Outline each blood parasite and name the species.
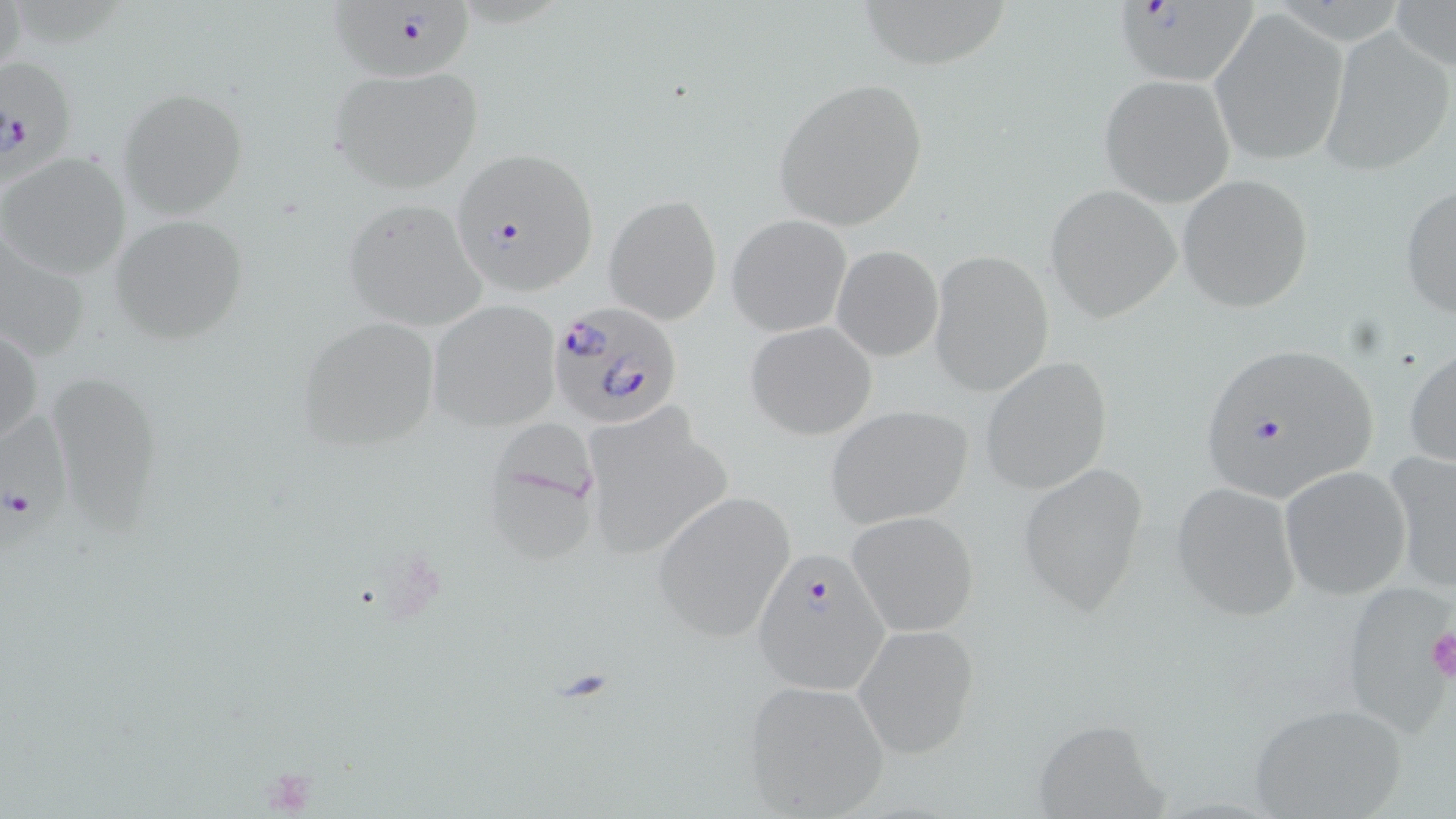

Approximate bounding boxes as [x1, y1, x2, y2] in pixels.
Plasmodium falciparum-infected red blood cells: [331, 2, 476, 83], [1117, 2, 1268, 92], [1, 47, 82, 186], [450, 147, 598, 298], [545, 300, 683, 430], [1195, 342, 1381, 504], [0, 410, 72, 564], [751, 548, 889, 693].
No Plasmodium ovale, Plasmodium malariae, Plasmodium vivax, Babesia divergens, or Trypanosoma brucei observed.

Summary:
  - Platelet locations: [1429, 628, 1456, 682], [258, 765, 318, 812]
  - Uninfected red blood cell locations: [848, 0, 1016, 68], [1388, 0, 1456, 72], [1209, 12, 1347, 165], [1319, 25, 1454, 176], [328, 64, 484, 194], [1100, 74, 1235, 205], [771, 77, 928, 233], [116, 88, 249, 219], [0, 152, 131, 280], [1176, 175, 1314, 312], [1044, 184, 1180, 321], [1400, 184, 1456, 320], [604, 194, 723, 326], [341, 198, 489, 328], [727, 214, 852, 336], [109, 215, 246, 344], [0, 233, 93, 366], [831, 245, 943, 361], [929, 249, 1053, 396], [429, 301, 560, 432], [296, 316, 441, 451], [744, 320, 879, 440], [1, 325, 43, 449], [1404, 345, 1456, 470], [979, 357, 1111, 495], [48, 374, 164, 536], [826, 404, 974, 529], [580, 405, 736, 562], [491, 412, 605, 570], [1386, 452, 1456, 593], [1015, 462, 1151, 614], [1279, 466, 1411, 600], [1170, 480, 1303, 621], [652, 490, 796, 642], [847, 510, 979, 637], [1336, 582, 1452, 731], [854, 624, 982, 759], [740, 678, 890, 817], [1244, 703, 1409, 818], [1030, 718, 1170, 819]
  - Slide-level diagnosis: Plasmodium falciparum
  - Magnification: 1000x
  - Image size: 1456×819 pixels
  - Preparation: thin blood smear
  - Field of view: single
  - Modality: light microscopy
  - Stain: May-Grünwald-Giemsa